Give the position of every Plasmodium parasite.
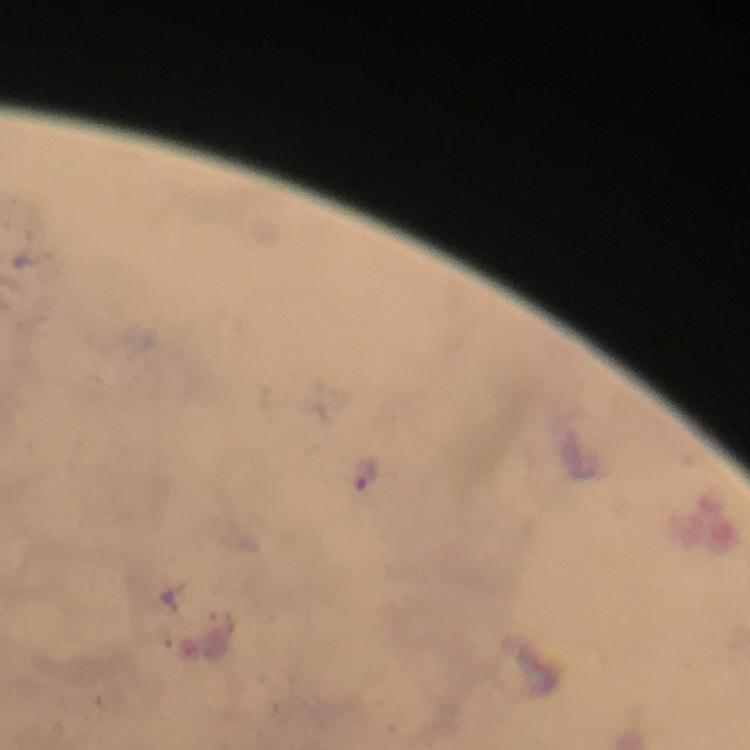

Approximate centers as {x, y} in pixels.
Plasmodium parasites: {367, 478}.

Summary:
  - Stain: Giemsa
  - Capture: smartphone photograph through a microscope
  - Magnification: 100x
  - Preparation: thick smear
  - Context: from a malaria diagnostic workup
  - Immersion oil: applied
  - Cropped from: one field of view
  - Image size: 750×750 pixels